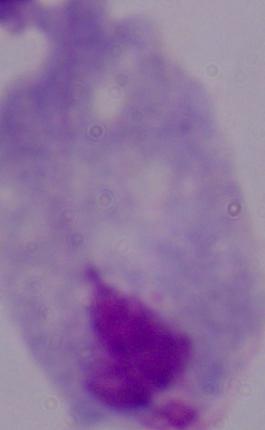

Summary:
  - Identification: trichomonad
  - Modality: photomicrograph
  - Magnification: 1000x